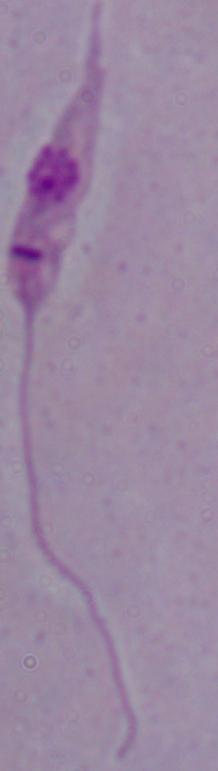

A Leishmania parasite is seen. Captured at 1000x magnification. Micrograph.